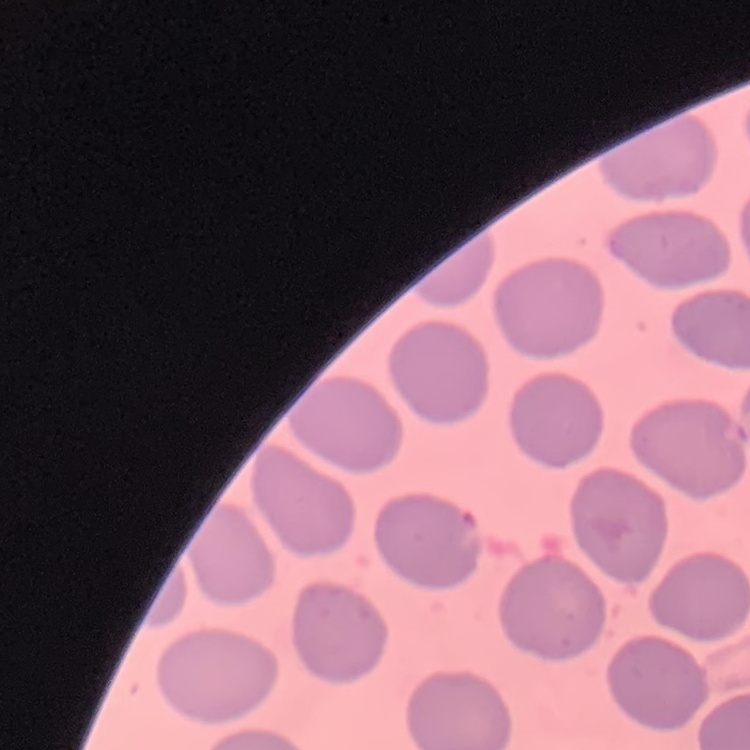

red blood cell morphology = no rouleaux formation
stain = Field's or Giemsa
image type = square crop of a larger photomicrograph
preparation = thin blood smear